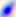
Photomicrograph. Captured at 400x magnification. Toxoplasma gondii is shown.